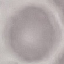
Result: no malaria parasites seen. Acquired by smartphone through the microscope eyepiece. Giemsa stain. Cell patch, automatically extracted from a larger field of view and resized to 64 × 64 pixels. Thin blood film.